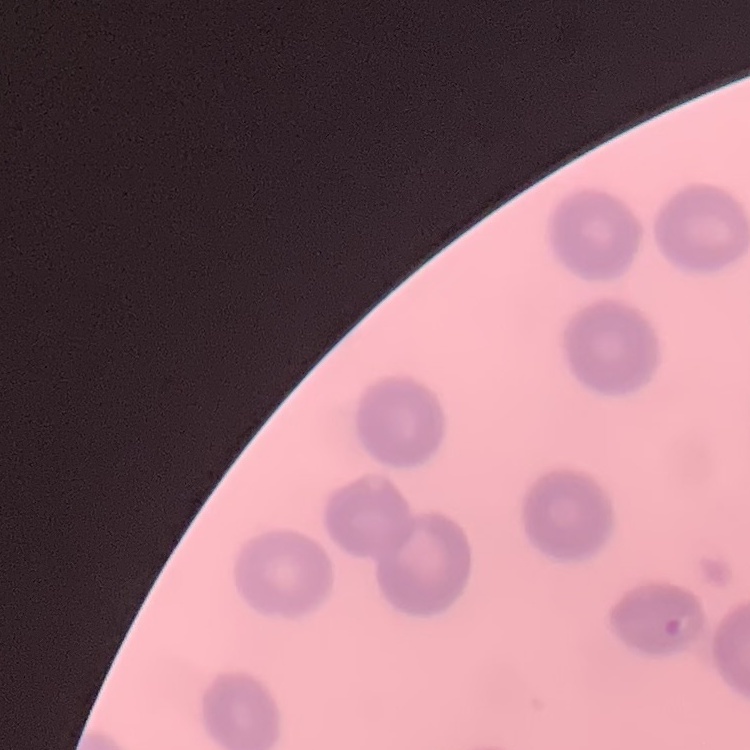

Summary:
  - Red blood cell morphology: no rouleaux formation
  - Image type: one tile cut from a larger photomicrograph
  - Preparation: thin peripheral smear
  - Stain: Field's or Giemsa